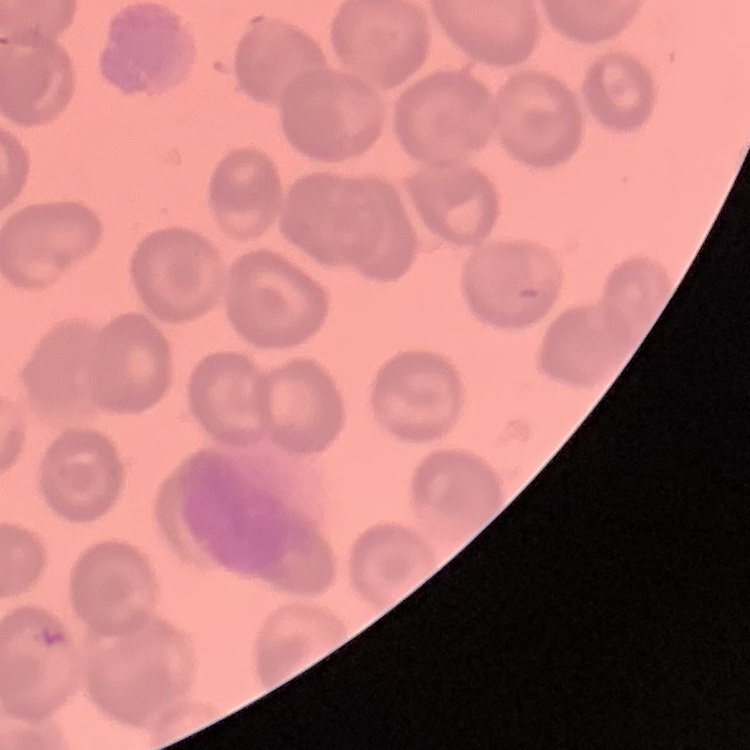 The red blood cells show no rouleaux formation. One tile cut from a larger photomicrograph. Field's or Giemsa stain. Thin blood smear.